Classify this cell by malaria status.
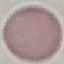

It is uninfected.

Giemsa-stained preparation. Thin smear of blood. Cell patch, automatically extracted from a larger field of view and resized to 64 × 64 pixels. Acquired by smartphone through the microscope eyepiece.